Outline each blood parasite and name the species.
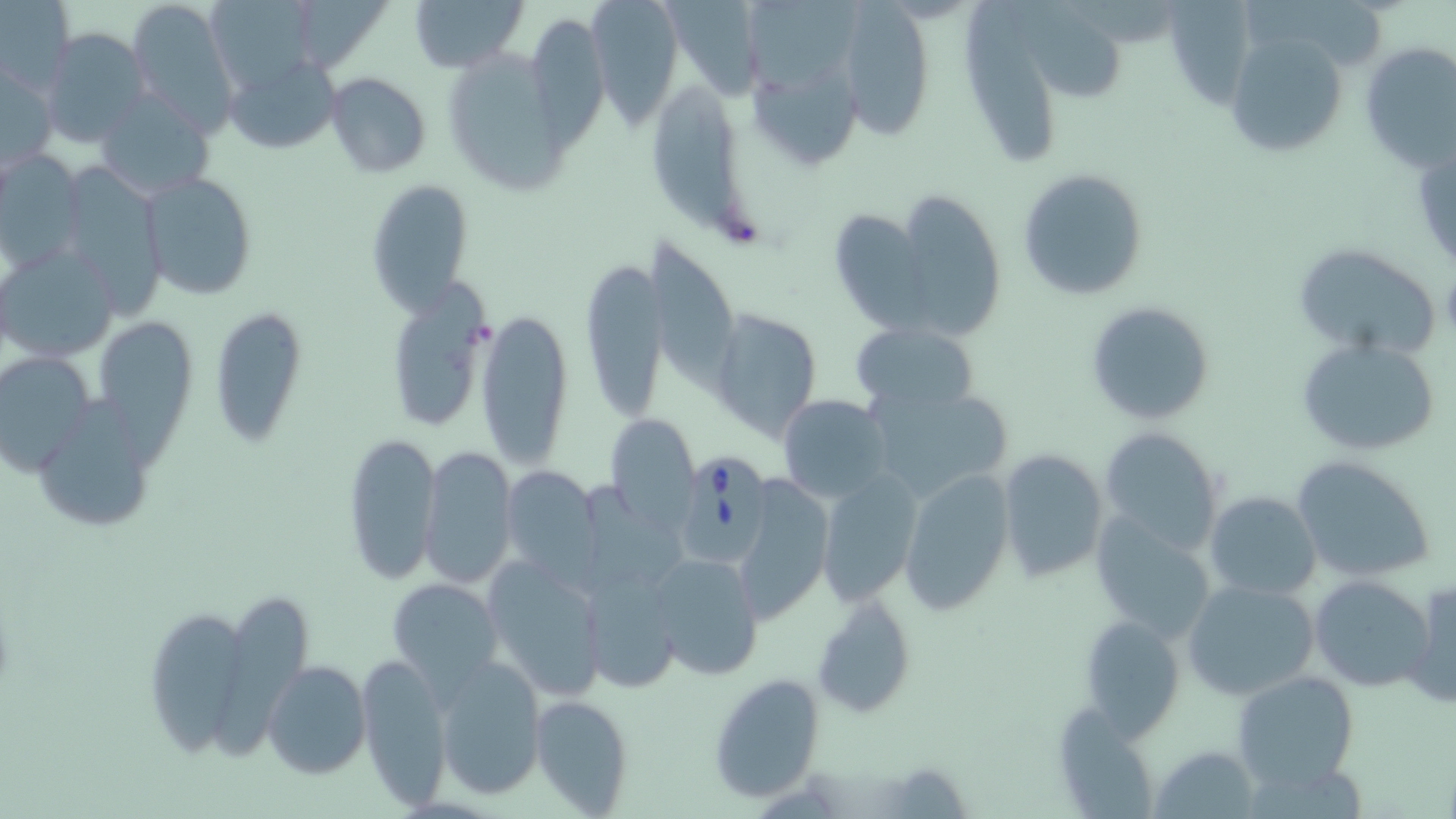

Approximate bounding boxes as named x1/y1/x2/y2 corners in pixels.
Babesia divergens-infected red blood cells: (x1=668, y1=444, x2=776, y2=573).
No Plasmodium falciparum, Plasmodium ovale, Plasmodium malariae, Plasmodium vivax, or Trypanosoma brucei observed.

Uninfected red blood cell locations: (x1=125, y1=0, x2=242, y2=133), (x1=407, y1=0, x2=527, y2=73), (x1=583, y1=0, x2=684, y2=124), (x1=0, y1=2, x2=73, y2=94), (x1=204, y1=2, x2=326, y2=93), (x1=1014, y1=2, x2=1129, y2=109), (x1=1245, y1=2, x2=1393, y2=72), (x1=660, y1=3, x2=763, y2=108), (x1=963, y1=3, x2=1061, y2=166), (x1=1161, y1=3, x2=1255, y2=113), (x1=839, y1=4, x2=934, y2=137), (x1=301, y1=5, x2=395, y2=68), (x1=745, y1=5, x2=862, y2=90), (x1=532, y1=17, x2=611, y2=159), (x1=41, y1=28, x2=150, y2=149), (x1=1221, y1=30, x2=1354, y2=160), (x1=1358, y1=40, x2=1455, y2=171), (x1=451, y1=50, x2=566, y2=199), (x1=222, y1=55, x2=338, y2=156), (x1=2, y1=65, x2=59, y2=173), (x1=752, y1=66, x2=860, y2=166), (x1=325, y1=72, x2=431, y2=178), (x1=655, y1=84, x2=743, y2=230), (x1=96, y1=88, x2=214, y2=200), (x1=1, y1=149, x2=86, y2=271), (x1=58, y1=167, x2=167, y2=317), (x1=1016, y1=167, x2=1148, y2=301), (x1=139, y1=171, x2=257, y2=302), (x1=364, y1=178, x2=475, y2=315), (x1=892, y1=187, x2=1005, y2=339), (x1=828, y1=209, x2=927, y2=328), (x1=649, y1=239, x2=740, y2=385), (x1=1, y1=240, x2=119, y2=362), (x1=1289, y1=242, x2=1442, y2=362), (x1=580, y1=255, x2=668, y2=422), (x1=384, y1=280, x2=495, y2=435), (x1=1085, y1=301, x2=1217, y2=427), (x1=210, y1=307, x2=308, y2=447), (x1=707, y1=307, x2=823, y2=443), (x1=476, y1=308, x2=574, y2=470), (x1=99, y1=314, x2=205, y2=471), (x1=851, y1=322, x2=981, y2=416), (x1=1298, y1=338, x2=1442, y2=456), (x1=0, y1=351, x2=95, y2=474), (x1=863, y1=382, x2=1014, y2=504), (x1=777, y1=393, x2=893, y2=504), (x1=32, y1=397, x2=158, y2=536), (x1=604, y1=413, x2=701, y2=529), (x1=1097, y1=428, x2=1225, y2=553), (x1=341, y1=430, x2=441, y2=586), (x1=418, y1=444, x2=517, y2=591), (x1=995, y1=448, x2=1109, y2=585), (x1=1291, y1=454, x2=1435, y2=582), (x1=501, y1=466, x2=602, y2=581), (x1=813, y1=469, x2=923, y2=608), (x1=898, y1=469, x2=1016, y2=616), (x1=731, y1=477, x2=834, y2=624), (x1=1205, y1=491, x2=1320, y2=601), (x1=1092, y1=514, x2=1218, y2=645), (x1=647, y1=552, x2=766, y2=681), (x1=483, y1=558, x2=607, y2=700), (x1=580, y1=568, x2=681, y2=695), (x1=1308, y1=573, x2=1436, y2=695), (x1=1404, y1=577, x2=1456, y2=709), (x1=387, y1=578, x2=503, y2=692), (x1=1181, y1=579, x2=1320, y2=702), (x1=217, y1=595, x2=320, y2=765), (x1=811, y1=595, x2=916, y2=716), (x1=146, y1=609, x2=247, y2=763), (x1=1080, y1=614, x2=1188, y2=736), (x1=357, y1=652, x2=453, y2=808), (x1=435, y1=658, x2=546, y2=798), (x1=263, y1=660, x2=370, y2=780), (x1=1233, y1=670, x2=1359, y2=787), (x1=707, y1=672, x2=828, y2=801), (x1=528, y1=694, x2=635, y2=816), (x1=1055, y1=701, x2=1154, y2=817), (x1=1147, y1=746, x2=1259, y2=817), (x1=868, y1=761, x2=974, y2=817). Slide-level diagnosis: Babesia divergens. May-Grünwald-Giemsa-stained preparation. Image is 1456×819 pixels. Optical microscopy. One field of a larger specimen. Thin blood film. Captured at 1000x magnification.